Locate every Plasmodium parasite.
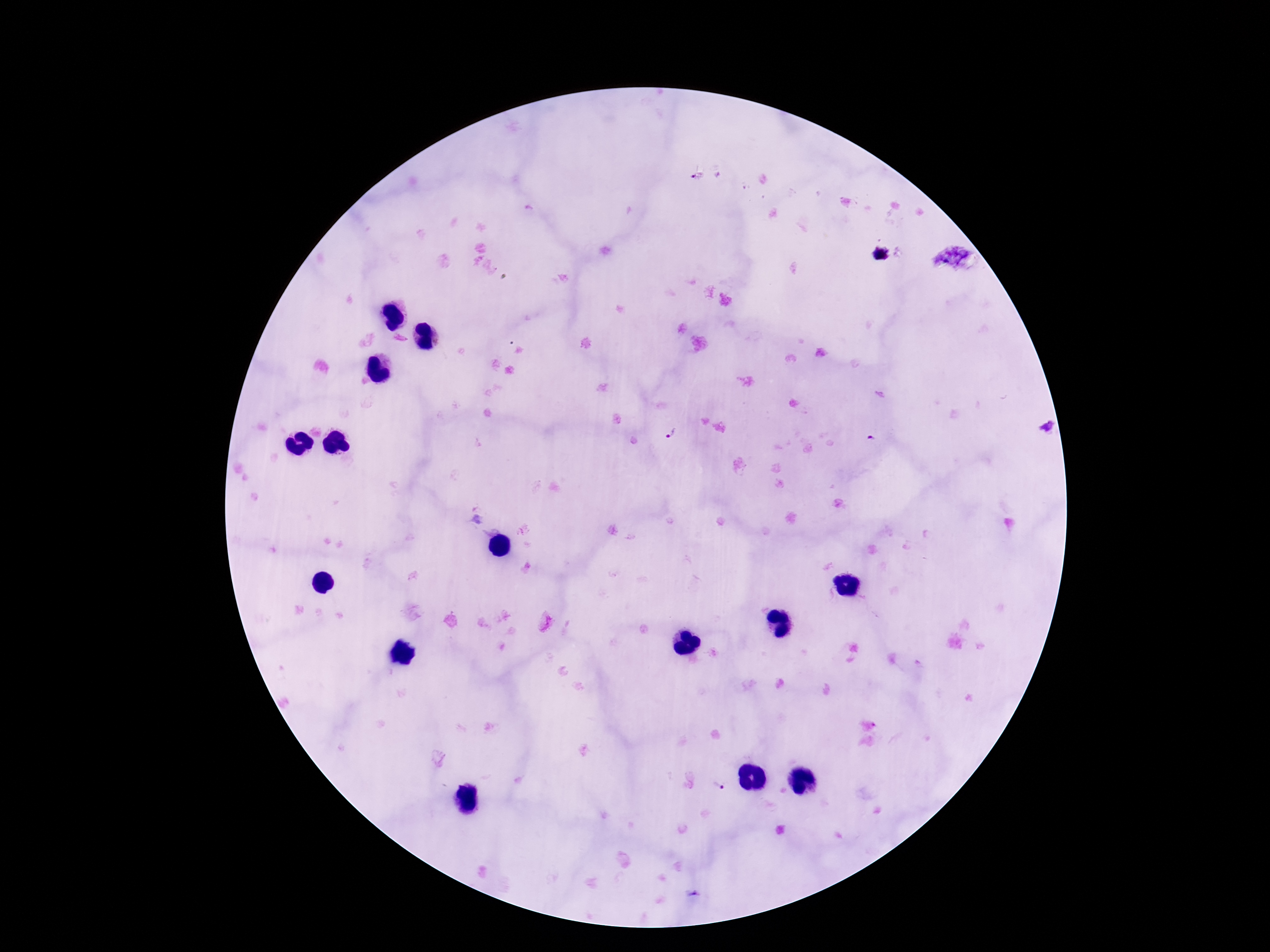

Approximate centers as [x, y] in pixels.
Plasmodium parasites: [879, 254], [671, 433], [872, 438], [719, 786].

Single field of view. Smartphone photograph taken through the microscope eyepiece. Thick blood film. Giemsa-stained preparation. Patient malaria status: infected. 100x magnification. Image is 1270×952 pixels.